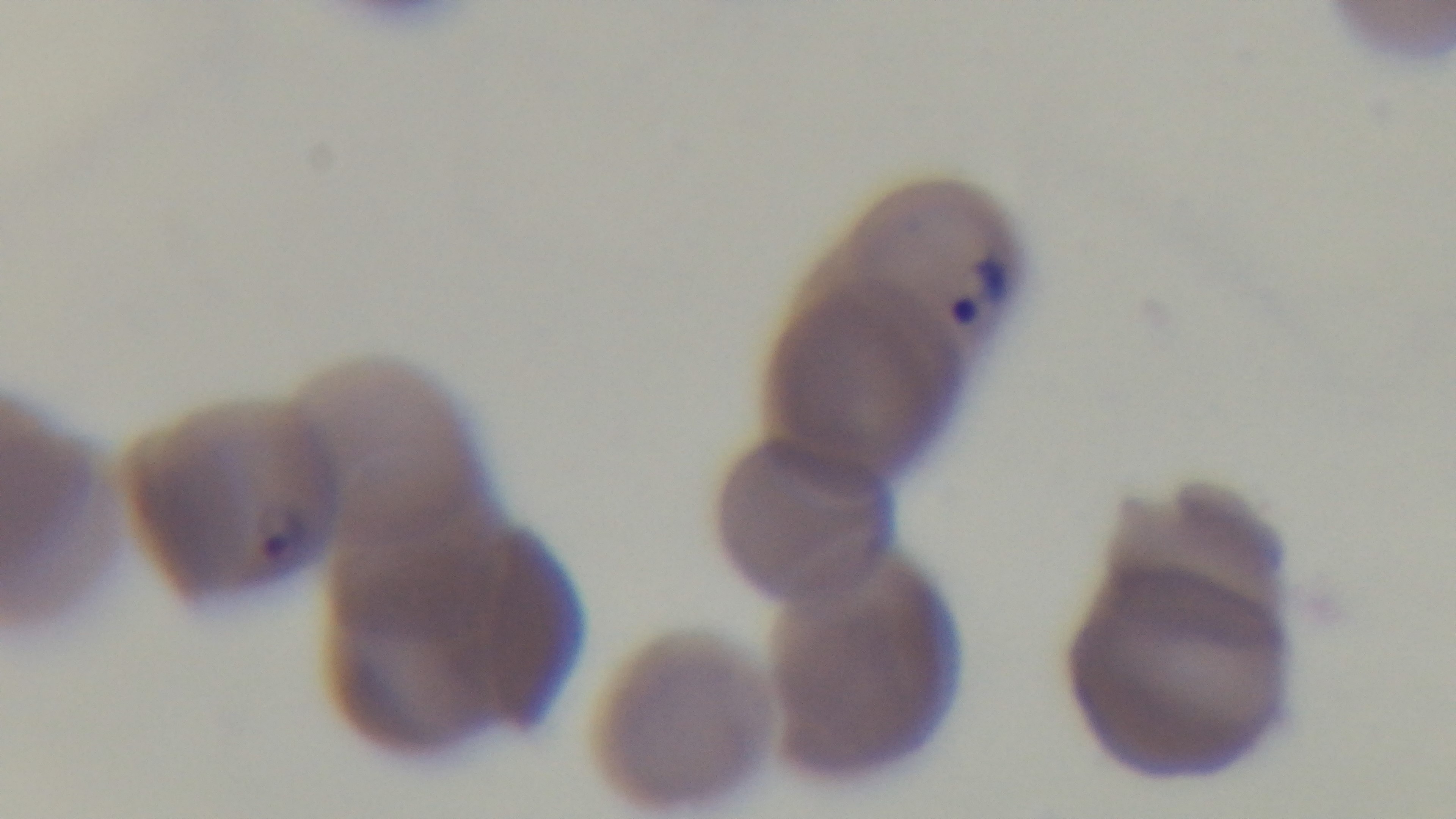 Preparation: thin smear. Giemsa-stained. Single field of view. Light microscopy. Malaria status: positive. Oil-immersion objective, 100x. Mounted 4K digital camera.